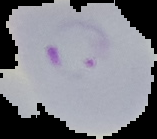 From a thin blood film. Image is 157×139 pixels. Malaria status: parasitized. Segmented cell region on a black background.